Locate every blood parasite and identify its species.
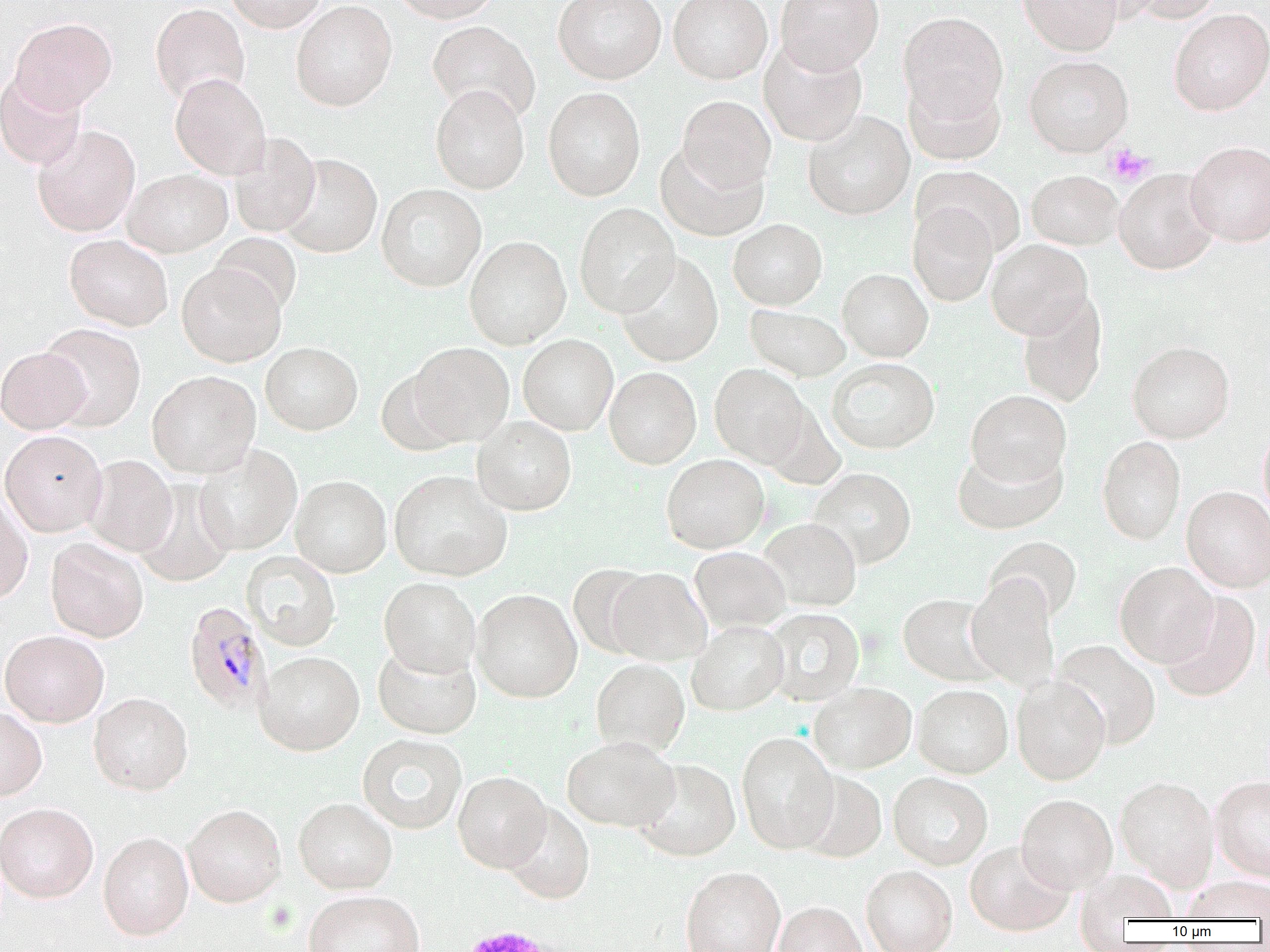
Approximate bounding boxes as (x1,y1)-(x2,y2) corner pairs in pixels.
Plasmodium malariae-infected red blood cells: (183,601)-(271,713).
No Plasmodium falciparum, Plasmodium ovale, Plasmodium vivax, Babesia divergens, or Trypanosoma brucei observed.

Summary:
  - Uninfected red blood cell locations: (223,0)-(327,33), (389,0)-(502,23), (553,0)-(666,84), (668,0)-(773,84), (775,0)-(884,74), (1018,0)-(1123,55), (1128,0)-(1222,23), (291,1)-(397,111), (150,3)-(250,105), (1168,8)-(1270,116), (898,12)-(1008,120), (9,18)-(117,113), (428,20)-(540,123), (759,37)-(867,147), (1024,55)-(1133,157), (0,72)-(87,170), (170,73)-(271,180), (904,74)-(1006,166), (431,85)-(530,194), (543,87)-(645,201), (677,95)-(776,192), (803,111)-(915,220), (32,125)-(140,236), (228,132)-(321,237), (1185,141)-(1270,246), (655,142)-(769,242), (279,153)-(383,258), (913,165)-(1025,257), (123,168)-(233,257), (1113,168)-(1220,274), (1026,170)-(1123,250), (376,183)-(486,292), (574,202)-(680,318), (908,203)-(998,307), (728,219)-(827,310), (210,233)-(301,317), (64,234)-(173,331), (464,235)-(571,349), (986,239)-(1093,339), (616,252)-(724,367), (176,262)-(286,367), (837,268)-(933,362), (1017,291)-(1108,408), (745,304)-(850,381), (40,322)-(147,431), (518,334)-(618,436), (1127,341)-(1235,443), (260,342)-(363,435), (409,342)-(514,446), (0,347)-(90,434), (827,358)-(940,455), (709,363)-(811,468), (604,366)-(701,469), (376,368)-(466,456), (147,370)-(261,478), (965,390)-(1071,488), (472,417)-(576,516), (1258,424)-(1270,525), (0,430)-(108,536), (1097,436)-(1185,544), (193,444)-(302,555), (952,445)-(1067,534), (661,454)-(769,553), (84,455)-(178,556), (808,467)-(917,569), (388,470)-(512,581), (290,475)-(392,578), (135,480)-(235,588), (1182,486)-(1270,591), (0,493)-(33,602), (758,518)-(862,611), (985,536)-(1082,623), (45,538)-(148,642), (689,547)-(791,632), (242,550)-(341,651), (1115,561)-(1218,667), (568,564)-(656,658), (605,568)-(712,666), (966,575)-(1060,691), (379,577)-(481,677), (471,588)-(582,703), (1158,591)-(1260,702), (898,594)-(1001,686), (763,608)-(864,706), (687,620)-(789,715), (1,630)-(109,727), (1053,639)-(1161,748), (372,643)-(481,739), (255,650)-(364,755), (591,659)-(690,756), (1011,677)-(1111,784), (808,682)-(916,773), (913,684)-(1013,778), (88,692)-(193,795), (0,707)-(47,800), (736,732)-(839,853), (357,734)-(467,834), (561,737)-(680,832), (633,759)-(741,861), (797,770)-(887,863), (453,771)-(552,872), (888,772)-(993,870), (1210,775)-(1270,881), (1116,776)-(1220,889), (1016,794)-(1117,894), (293,797)-(397,894), (0,802)-(98,903), (501,803)-(595,904), (183,804)-(286,907), (98,831)-(194,940), (964,840)-(1075,937), (861,865)-(958,952), (681,866)-(786,952), (1077,870)-(1180,926), (1182,877)-(1270,922), (303,890)-(425,952), (773,901)-(868,952)
  - Platelet locations: (1104,144)-(1154,186), (455,923)-(565,951)
  - Slide-level diagnosis: Plasmodium malariae
  - Field of view: single
  - Image size: 1270×952 pixels
  - Modality: optical microscopy
  - Magnification: 1000x
  - Preparation: thin blood smear